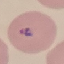
Result: malaria parasites detected. Acquired by smartphone through the microscope eyepiece. Thin smear of blood. Giemsa-stained preparation. Cell patch, automatically extracted from a larger field of view and resized to 64 × 64 pixels.